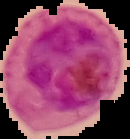
Summary:
  - Preparation: thin blood film
  - Result: Plasmodium parasites detected
  - Image type: segmented cell region with the area outside set to black
  - Image size: 130×139 pixels